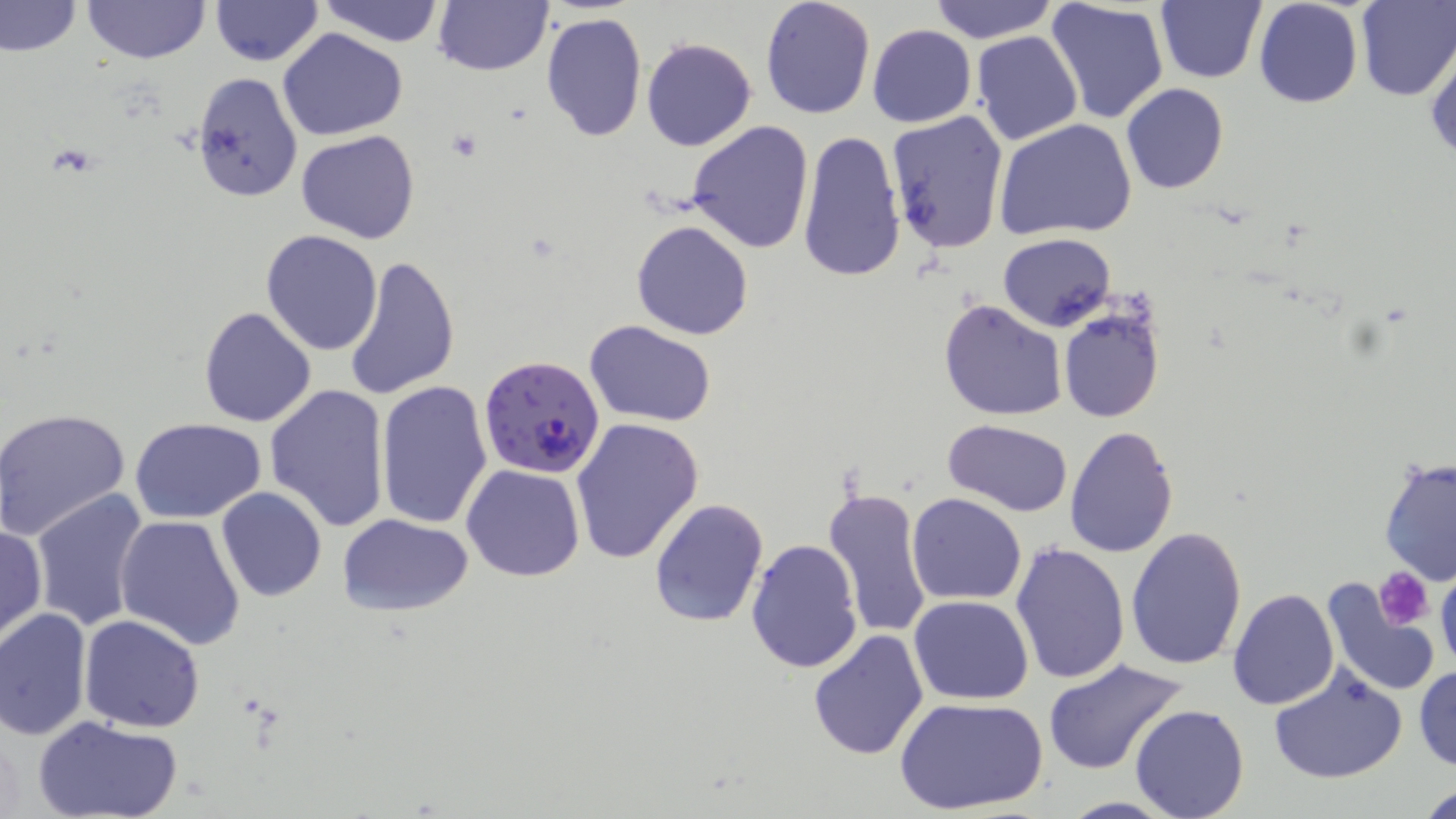

Summary:
  - Coordinate format: approximate bounding boxes as (x1, y1, x2, y2) in pixels
  - Platelet locations: (1375, 566, 1433, 630)
  - Plasmodium falciparum-infected red blood cell locations: (478, 356, 607, 479)
  - Uninfected red blood cell locations: (82, 0, 209, 64), (315, 0, 445, 46), (433, 0, 553, 75), (760, 0, 877, 121), (926, 0, 1060, 43), (1156, 0, 1267, 85), (1254, 0, 1363, 108), (1354, 0, 1455, 101), (0, 1, 82, 59), (209, 1, 324, 66), (1045, 2, 1168, 125), (540, 11, 647, 142), (867, 25, 976, 127), (278, 28, 408, 141), (970, 31, 1083, 146), (641, 36, 757, 152), (1426, 46, 1456, 163), (189, 71, 303, 203), (1120, 83, 1229, 195), (886, 111, 1010, 255), (686, 119, 815, 254), (994, 119, 1136, 240), (286, 124, 406, 355), (296, 129, 419, 243), (797, 129, 907, 284), (630, 219, 754, 340), (259, 230, 383, 355), (997, 233, 1115, 331), (343, 253, 459, 402), (208, 254, 372, 419), (939, 299, 1068, 420), (199, 306, 317, 428), (1058, 307, 1166, 424), (584, 320, 717, 425), (373, 380, 492, 530), (264, 383, 390, 531), (0, 407, 132, 540), (571, 417, 704, 563), (131, 419, 265, 524), (942, 420, 1072, 516), (1063, 426, 1179, 558), (1379, 455, 1456, 587), (461, 463, 586, 583), (823, 485, 933, 641), (216, 487, 327, 601), (30, 489, 154, 633), (907, 493, 1028, 604), (648, 497, 771, 629), (336, 511, 476, 617), (114, 515, 246, 650), (0, 521, 47, 644), (1126, 527, 1249, 670), (745, 539, 864, 674), (1008, 543, 1131, 686), (1435, 566, 1456, 680), (1319, 577, 1441, 699), (1228, 590, 1338, 710), (909, 595, 1033, 704), (0, 607, 92, 739), (78, 615, 205, 732), (807, 628, 928, 760), (1042, 659, 1187, 776), (1413, 664, 1456, 771), (1267, 665, 1409, 784), (897, 697, 1048, 817), (1130, 703, 1250, 819), (33, 714, 183, 819), (1418, 782, 1456, 818)
  - Slide-level diagnosis: Plasmodium falciparum
  - Preparation: thin blood film
  - Image size: 1456×819 pixels
  - Modality: light microscopy
  - Magnification: 1000x
  - Field of view: single
  - Stain: May-Grünwald-Giemsa